Locate every leukocyte (white blood cell).
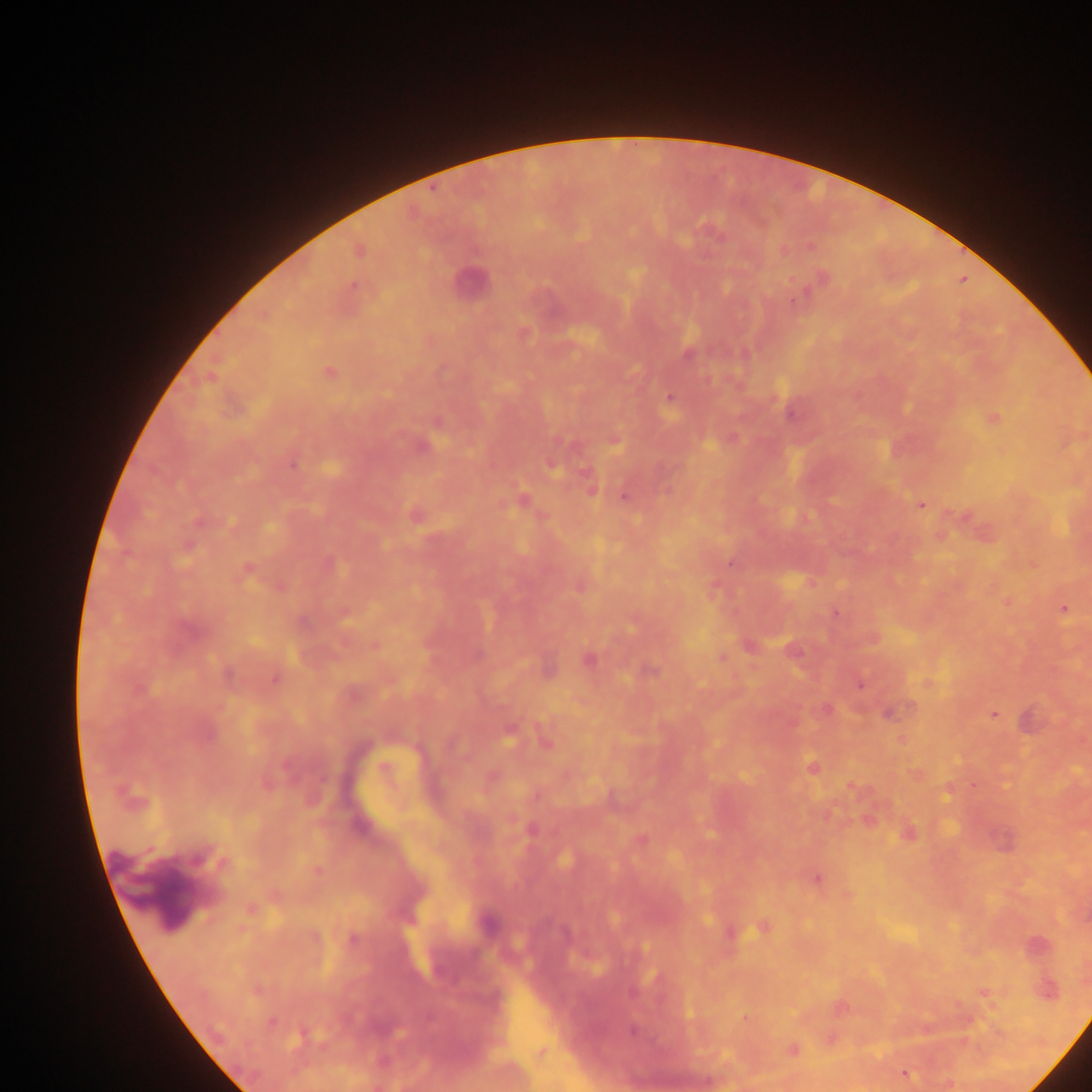
No leukocytes observed.

capture = mobile-phone photograph through a microscope
Plasmodium parasite locations = approximate centers as {x, y} in pixels: {434, 189}, {963, 281}, {353, 282}, {791, 300}, {688, 355}, {326, 372}, {670, 397}, {291, 464}, {623, 495}, {523, 499}, {922, 504}, {730, 564}, {245, 569}, {281, 587}, {1062, 607}, {836, 612}, {721, 658}, {589, 659}, {276, 677}, {861, 686}, {993, 714}, {812, 767}, {974, 785}, {849, 788}, {815, 878}, {251, 909}, {731, 934}, {352, 939}, {985, 991}, {745, 1017}, {793, 1049}, {904, 1073}
image size = 1092×1092 pixels
preparation = thick blood film
country = Ghana
field of view = single